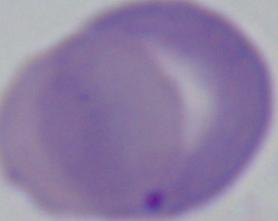 Photomicrograph. A Babesia parasite is shown. 1000x magnification.